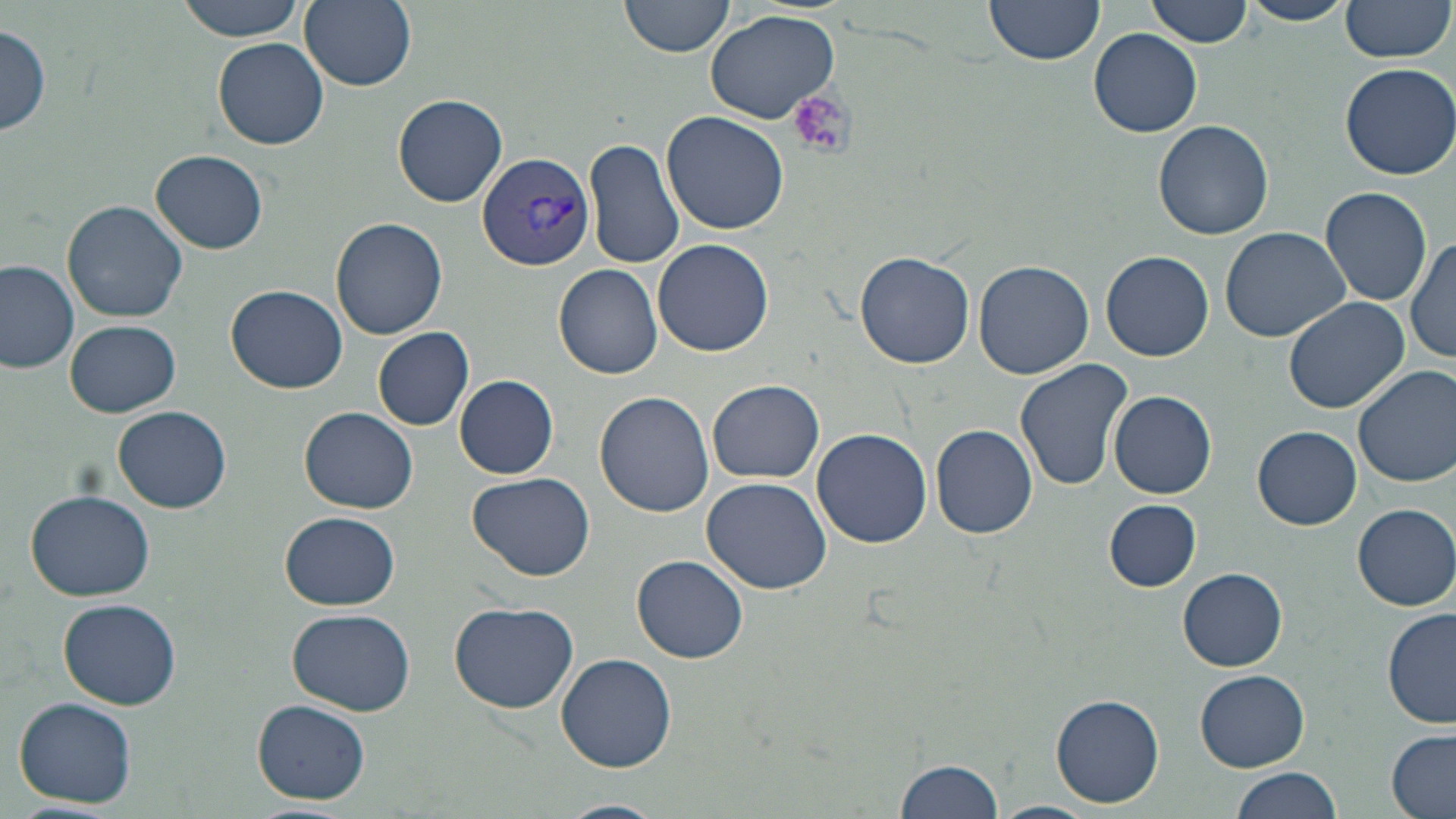

slide_level_diagnosis: Plasmodium vivax
field_of_view: single
magnification: 1000x
platelet_locations: 'approximate bounding boxes as (x1, y1, x2, y2) in pixels: (789, 92, 854, 160)'
modality: light microscopy
stain: May-Grünwald-Giemsa
uninfected_red_blood_cell_locations: 'approximate bounding boxes as (x1, y1, x2, y2) in pixels: (173, 0, 306, 40), (299, 0, 416, 90), (619, 0, 734, 58), (985, 0, 1107, 69), (1147, 0, 1252, 48), (1237, 0, 1354, 27), (1337, 1, 1453, 65), (703, 9, 844, 127), (0, 23, 52, 137), (1089, 28, 1202, 136), (211, 37, 329, 150), (1340, 62, 1456, 179), (392, 93, 508, 207), (662, 110, 790, 236), (1154, 119, 1275, 239), (585, 136, 683, 270), (152, 150, 269, 252), (1320, 186, 1432, 310), (63, 200, 187, 322), (331, 216, 448, 340), (1220, 227, 1351, 344), (1407, 233, 1456, 365), (653, 239, 775, 355), (1102, 250, 1213, 361), (856, 252, 975, 368), (0, 260, 79, 375), (973, 260, 1094, 379), (554, 264, 663, 381), (227, 284, 348, 393), (1282, 295, 1410, 413), (65, 319, 181, 417), (372, 327, 475, 431), (1014, 358, 1133, 491), (1354, 363, 1456, 487), (456, 375, 558, 479), (709, 379, 823, 484), (595, 390, 715, 518), (1108, 390, 1217, 498), (114, 405, 232, 513), (300, 405, 419, 513), (930, 423, 1040, 539), (1253, 426, 1361, 530), (812, 427, 932, 548), (468, 471, 596, 581), (701, 476, 832, 595), (23, 489, 154, 602), (1103, 498, 1201, 592), (1352, 503, 1456, 609), (279, 512, 401, 610), (633, 555, 749, 664), (1178, 568, 1287, 671), (59, 599, 181, 710), (448, 602, 579, 714), (286, 607, 416, 716), (1381, 607, 1455, 729), (555, 652, 677, 773), (1195, 670, 1310, 771), (1051, 693, 1164, 807), (13, 697, 137, 809), (253, 698, 370, 804), (1386, 731, 1455, 819), (892, 756, 1005, 819), (1231, 765, 1344, 819), (555, 799, 665, 819), (989, 801, 1100, 819)'
plasmodium_vivax_infected_red_blood_cell_locations: 'approximate bounding boxes as (x1, y1, x2, y2) in pixels: (476, 149, 595, 273)'
image_size: 1456×819 pixels
preparation: thin blood smear